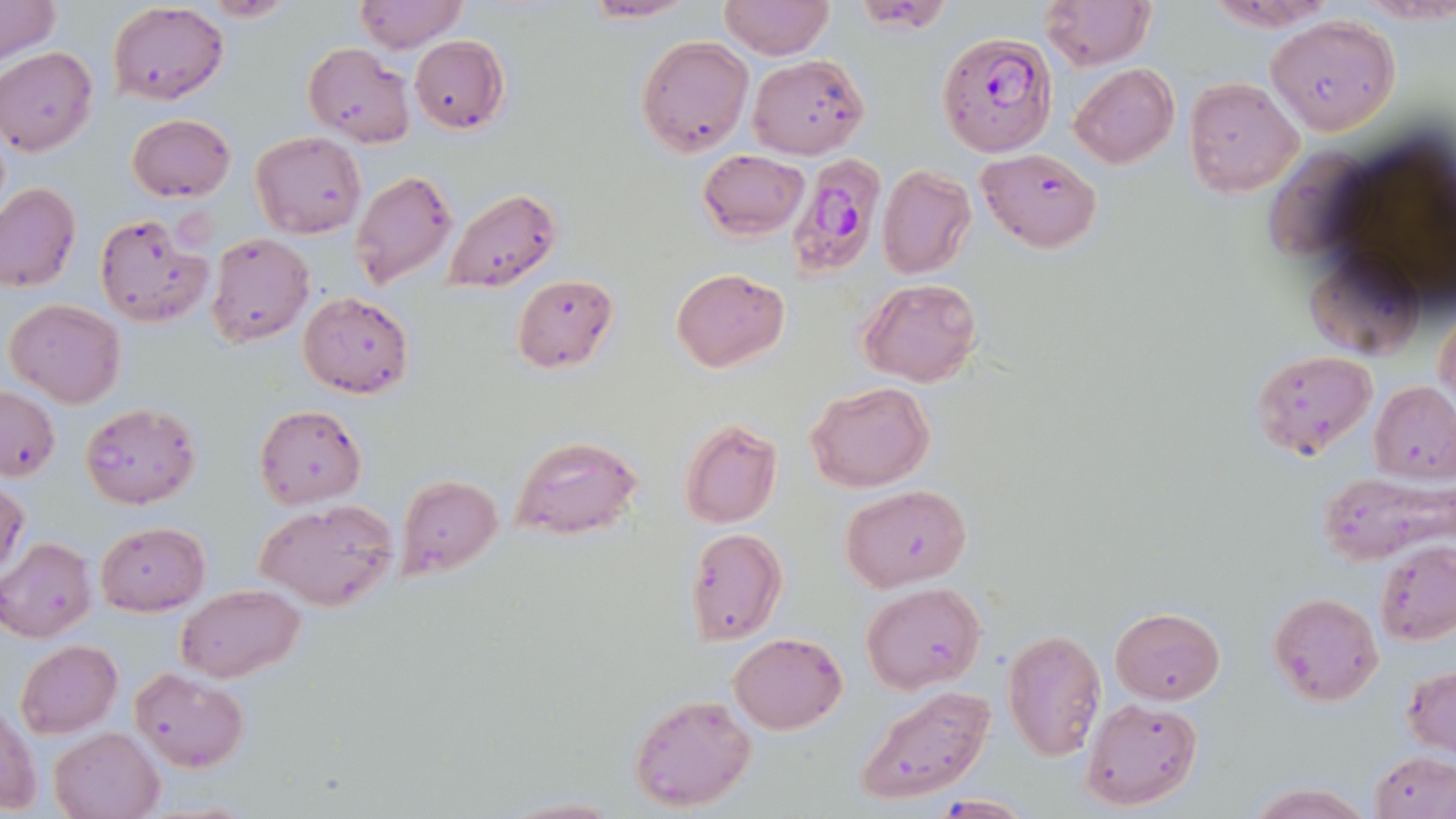
Approximate bounding boxes as (x1,y1)-(x2,y2) corner pairs in pixels. Plasmodium falciparum-infected red blood cell locations: (938,32)-(1057,155), (784,155)-(882,281). Uninfected red blood cell locations: (0,0)-(60,63), (190,0)-(298,21), (354,0)-(467,53), (579,0)-(702,22), (717,0)-(835,60), (1041,0)-(1153,71), (1202,0)-(1341,32), (107,3)-(229,106), (1265,13)-(1402,135), (408,36)-(509,131), (635,36)-(754,156), (301,42)-(416,147), (0,47)-(99,156), (748,55)-(869,158), (1068,64)-(1179,168), (1183,77)-(1305,198), (126,113)-(234,202), (250,132)-(366,239), (697,148)-(810,239), (978,148)-(1102,252), (1263,148)-(1374,259), (876,165)-(976,279), (351,170)-(459,289), (1,182)-(81,293), (443,188)-(561,292), (93,212)-(213,328), (207,232)-(314,346), (1305,247)-(1429,360), (671,268)-(789,372), (513,272)-(620,373), (858,278)-(983,387), (298,291)-(415,399), (1433,297)-(1456,423), (5,298)-(126,407), (1251,349)-(1378,463), (805,381)-(933,493), (1369,383)-(1456,481), (1,384)-(60,481), (79,401)-(201,509), (255,403)-(368,510), (679,418)-(783,529), (510,434)-(645,541), (1320,471)-(1453,565), (397,474)-(504,578), (0,480)-(29,580), (840,484)-(972,591), (255,500)-(399,610), (95,521)-(210,617), (685,528)-(788,645), (0,538)-(97,643), (1375,543)-(1456,647), (178,583)-(306,682), (859,583)-(986,692), (1269,592)-(1383,705), (1111,607)-(1225,705), (1001,627)-(1106,760), (729,633)-(847,734), (15,639)-(122,737), (1403,664)-(1456,756), (131,666)-(249,772), (854,684)-(996,806), (627,693)-(757,812), (1080,698)-(1204,810), (1,702)-(41,817), (51,728)-(163,819), (1372,751)-(1455,819), (1244,781)-(1372,818), (930,794)-(1035,817), (496,796)-(626,819). Slide-level diagnosis: Plasmodium falciparum. May-Grünwald-Giemsa stain. Thin blood film. One field of a larger specimen. Optical microscopy. Image is 1456×819 pixels. Captured at 1000x magnification.